Give the extent of all uninfected red blood cells.
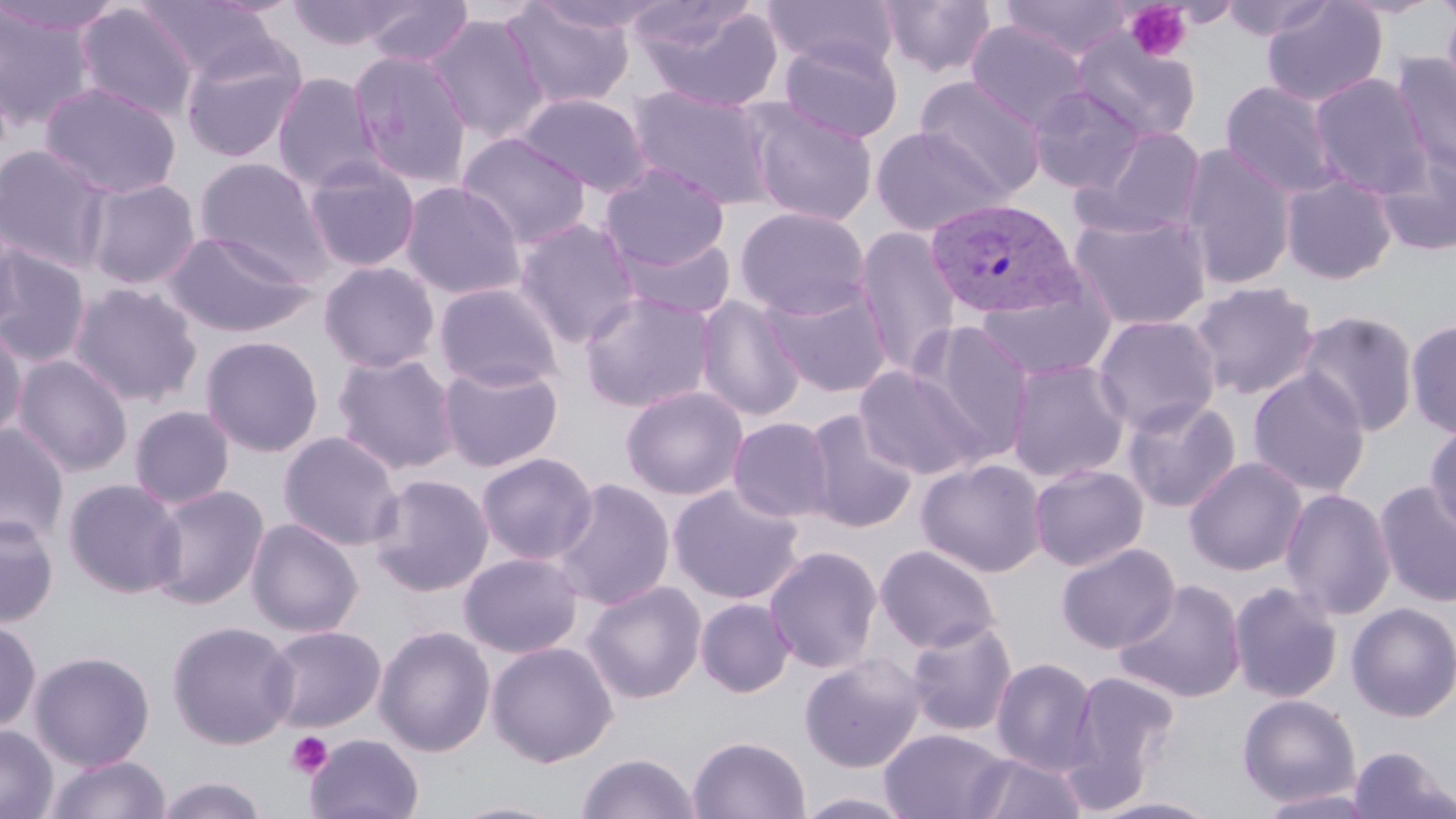
Approximate bounding boxes as [x1, y1, x2, y2] in pixels.
Uninfected red blood cells: [0, 0, 124, 37], [135, 0, 284, 83], [285, 0, 415, 51], [360, 0, 474, 67], [762, 0, 898, 73], [877, 0, 998, 79], [1000, 0, 1134, 61], [1217, 0, 1336, 42], [1261, 0, 1388, 108], [1333, 0, 1446, 19], [1440, 0, 1456, 106], [633, 1, 785, 112], [502, 2, 635, 112], [74, 3, 200, 123], [0, 4, 98, 130], [423, 14, 550, 143], [965, 21, 1089, 130], [1072, 30, 1202, 144], [778, 36, 904, 144], [179, 38, 308, 164], [348, 50, 472, 188], [1392, 52, 1456, 179], [272, 72, 384, 193], [1309, 73, 1431, 197], [915, 76, 1046, 199], [1220, 80, 1341, 199], [39, 82, 182, 200], [627, 85, 778, 209], [1027, 85, 1146, 195], [515, 93, 652, 197], [745, 101, 879, 227], [1079, 125, 1208, 238], [870, 126, 1013, 236], [457, 133, 592, 250], [1179, 144, 1297, 290], [0, 145, 113, 272], [1374, 150, 1456, 256], [194, 157, 332, 279], [303, 159, 421, 272], [600, 163, 729, 272], [1280, 173, 1398, 285], [82, 178, 201, 290], [399, 180, 526, 300], [734, 206, 870, 320], [1068, 211, 1212, 331], [0, 213, 26, 336], [512, 218, 643, 348], [853, 226, 962, 379], [163, 231, 317, 337], [615, 232, 736, 320], [0, 247, 92, 369], [319, 261, 440, 373], [761, 280, 893, 398], [1188, 280, 1321, 401], [433, 281, 564, 393], [68, 282, 202, 407], [975, 287, 1115, 382], [579, 292, 718, 412], [695, 296, 806, 422], [1295, 311, 1419, 436], [1092, 314, 1221, 435], [1405, 319, 1456, 438], [912, 320, 1036, 459], [0, 322, 28, 445], [200, 335, 324, 456], [332, 352, 461, 475], [12, 354, 133, 477], [1006, 359, 1131, 483], [437, 362, 563, 472], [855, 366, 987, 480], [1247, 369, 1371, 497], [621, 385, 748, 500], [1120, 398, 1242, 513], [129, 405, 235, 510], [802, 409, 918, 533], [727, 417, 836, 523], [1424, 420, 1456, 535], [0, 424, 70, 548], [278, 431, 404, 552], [476, 452, 598, 565], [1184, 457, 1307, 577], [917, 459, 1046, 577], [1029, 464, 1148, 571], [368, 473, 494, 596], [62, 478, 186, 599], [551, 478, 676, 610], [1374, 479, 1456, 609], [668, 483, 805, 605], [147, 484, 269, 610], [1279, 487, 1396, 621], [0, 513, 59, 628], [246, 517, 363, 638], [1056, 543, 1180, 654], [874, 544, 1001, 654], [763, 545, 883, 674], [458, 552, 584, 658], [1114, 579, 1247, 703], [582, 580, 706, 704], [1228, 581, 1344, 704], [695, 598, 795, 697], [1346, 601, 1456, 723], [0, 618, 42, 733], [904, 619, 1018, 737], [165, 620, 298, 750], [261, 625, 386, 733], [374, 625, 495, 758], [486, 641, 619, 767], [29, 649, 156, 771], [799, 653, 926, 773], [990, 657, 1099, 776], [1065, 670, 1181, 803], [1236, 693, 1361, 808], [0, 724, 58, 819], [879, 728, 1011, 818], [305, 733, 424, 819], [687, 735, 811, 819], [1347, 745, 1454, 819], [576, 752, 701, 819], [964, 752, 1088, 818], [44, 753, 171, 819], [153, 775, 271, 818], [1256, 789, 1383, 818], [793, 791, 919, 819], [1088, 796, 1224, 818], [443, 800, 570, 819].

slide-level diagnosis = Plasmodium vivax
magnification = 1000x
modality = light microscopy
field of view = one of a larger specimen
preparation = thin blood smear
platelet locations = approximate bounding boxes as [x1, y1, x2, y2] in pixels: [1124, 2, 1193, 62], [285, 731, 335, 779]
stain = May-Grünwald-Giemsa
Plasmodium vivax-infected red blood cell locations = approximate bounding boxes as [x1, y1, x2, y2] in pixels: [926, 198, 1083, 320]
image size = 1456×819 pixels